Identify the cell.
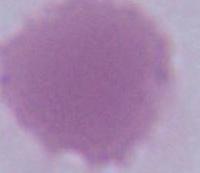

This is an erythrocyte.

Summary:
  - Magnification: 1000x
  - Modality: photomicrograph